Report the malaria status of this cell.
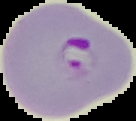
It is parasitized.

preparation = thin blood smear
image type = cell region segmented out of the field of view; surrounding area masked to black
image size = 136×121 pixels